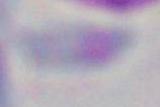
identification = Toxoplasma gondii
modality = micrograph
magnification = 1000x